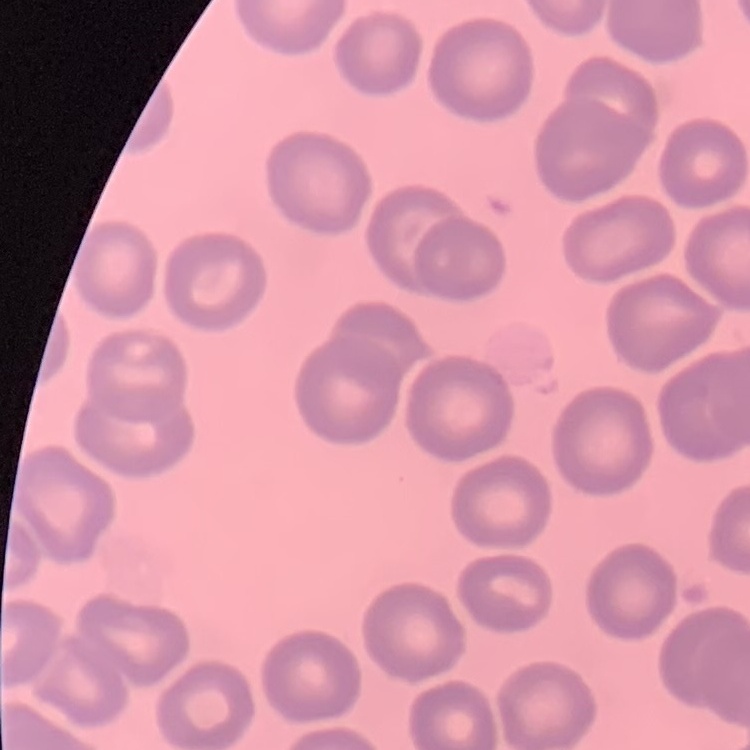
{
  "erythrocyte_morphology": "no rouleaux formation",
  "stain": "Field's or Giemsa",
  "image_type": "one tile cut from a larger photomicrograph",
  "preparation": "thin peripheral smear"
}